State which parasite is depicted.
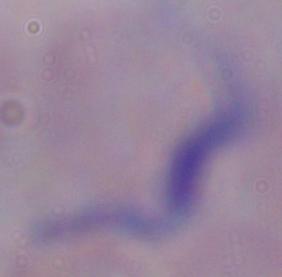
This is a trypanosome.

1000x magnification. Micrograph.